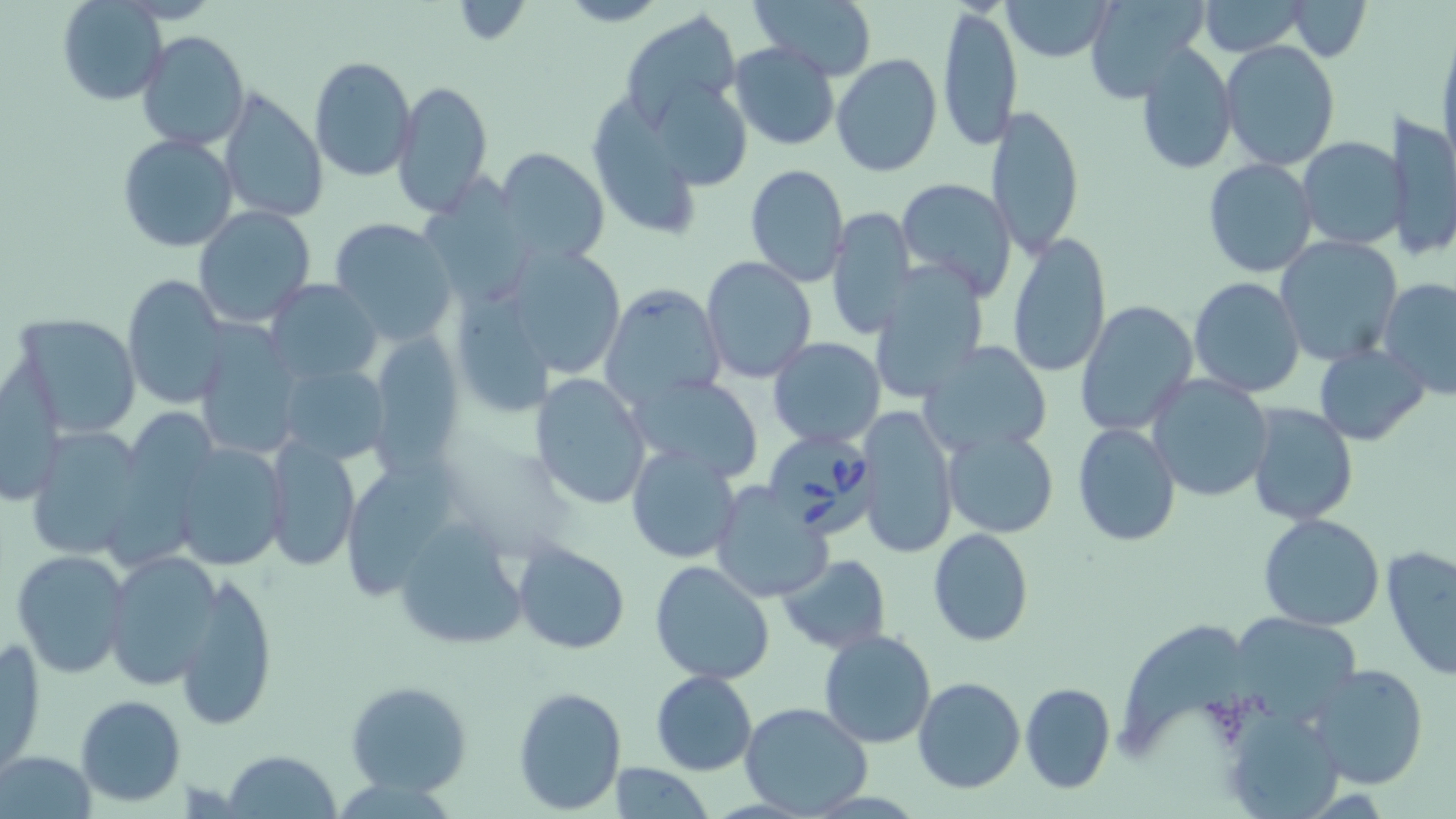

slide-level diagnosis = Babesia divergens
magnification = 1000x
image size = 1456×819 pixels
preparation = thin blood smear
field of view = single
uninfected red blood cell locations = approximate bounding boxes as [x1, y1, x2, y2] in pixels: [556, 0, 671, 27], [1001, 0, 1118, 61], [1083, 0, 1212, 102], [1193, 0, 1314, 56], [60, 1, 167, 105], [447, 1, 534, 46], [751, 1, 878, 79], [1285, 1, 1370, 61], [937, 4, 1023, 152], [622, 10, 741, 125], [138, 30, 249, 150], [1436, 33, 1456, 178], [730, 41, 841, 151], [1220, 41, 1339, 169], [1136, 44, 1237, 173], [830, 53, 942, 177], [309, 55, 416, 181], [393, 79, 494, 216], [217, 90, 328, 222], [582, 92, 719, 238], [986, 103, 1085, 260], [1390, 109, 1455, 262], [117, 134, 239, 254], [1298, 137, 1405, 251], [495, 146, 612, 268], [1202, 157, 1319, 278], [744, 163, 850, 287], [424, 169, 540, 306], [896, 178, 1017, 299], [193, 205, 316, 327], [826, 205, 916, 341], [328, 219, 456, 344], [1005, 232, 1112, 377], [1274, 235, 1404, 368], [514, 244, 623, 376], [701, 257, 816, 384], [870, 264, 986, 406], [121, 275, 229, 409], [1188, 276, 1306, 398], [264, 278, 381, 384], [1378, 279, 1456, 398], [599, 282, 727, 408], [1075, 300, 1199, 436], [13, 311, 143, 437], [193, 327, 305, 460], [367, 329, 463, 476], [768, 337, 887, 450], [916, 340, 1055, 460], [1314, 345, 1430, 446], [279, 360, 390, 465], [2, 365, 66, 505], [1146, 372, 1275, 502], [532, 373, 651, 510], [627, 373, 766, 483], [1246, 401, 1359, 524], [854, 406, 959, 561], [1072, 421, 1182, 548], [25, 427, 151, 562], [942, 427, 1058, 537], [262, 437, 360, 572], [172, 444, 289, 572], [625, 446, 742, 564], [711, 482, 833, 604], [1258, 513, 1385, 630], [393, 517, 532, 653], [927, 527, 1035, 647], [511, 539, 631, 655], [1382, 544, 1456, 682], [10, 547, 132, 679], [104, 551, 225, 690], [777, 554, 892, 654], [650, 559, 778, 686], [176, 571, 278, 730], [819, 630, 936, 749], [1, 641, 47, 779], [1305, 664, 1432, 789], [650, 671, 759, 775], [912, 676, 1025, 794], [344, 679, 475, 797], [1020, 682, 1115, 794], [512, 685, 625, 814], [76, 694, 186, 807], [739, 702, 874, 818], [1219, 705, 1348, 818], [225, 750, 340, 818], [3, 751, 96, 816], [609, 761, 713, 818]
stain = May-Grünwald-Giemsa
modality = light microscopy
Babesia divergens-infected red blood cell locations = approximate bounding boxes as [x1, y1, x2, y2] in pixels: [765, 432, 881, 540]